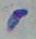

{
  "identification": "Toxoplasma gondii",
  "modality": "micrograph",
  "magnification": "1000x"
}